Report the malaria status of this cell.
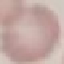
It is uninfected.

Summary:
  - Stain: Giemsa
  - Capture: smartphone camera at the microscope eyepiece
  - Preparation: thin blood smear
  - Image type: automatically extracted cell patch, resized to 64 × 64 pixels